Classify this cell by malaria status.
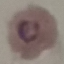
Parasitized.

{
  "stain": "Giemsa",
  "preparation": "thin blood smear",
  "image_type": "cell patch, automatically extracted from a larger field of view and resized to 64 × 64 pixels",
  "capture": "smartphone through the microscope eyepiece"
}